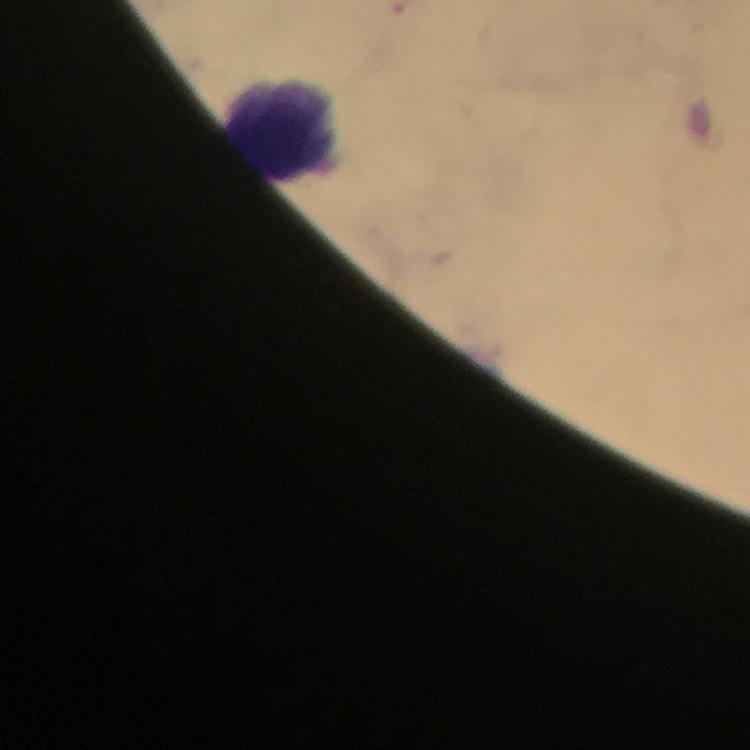
preparation: thick smear
cropped_from: one field of view
stain: Giemsa
context: from a diagnostic examination for malaria
image_size: 750×750 pixels
capture: smartphone photograph through a microscope
immersion_oil: used
leukocyte_locations: 'approximate centers as (x, y) in pixels: (286, 127)'
malaria_parasites: none seen
magnification: 100x